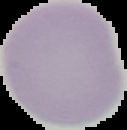
Summary:
  - Result: no malaria parasites detected
  - Preparation: thin blood film
  - Image type: segmented cell region on a black background
  - Image size: 127×130 pixels